Point out malaria parasites and leukocytes.
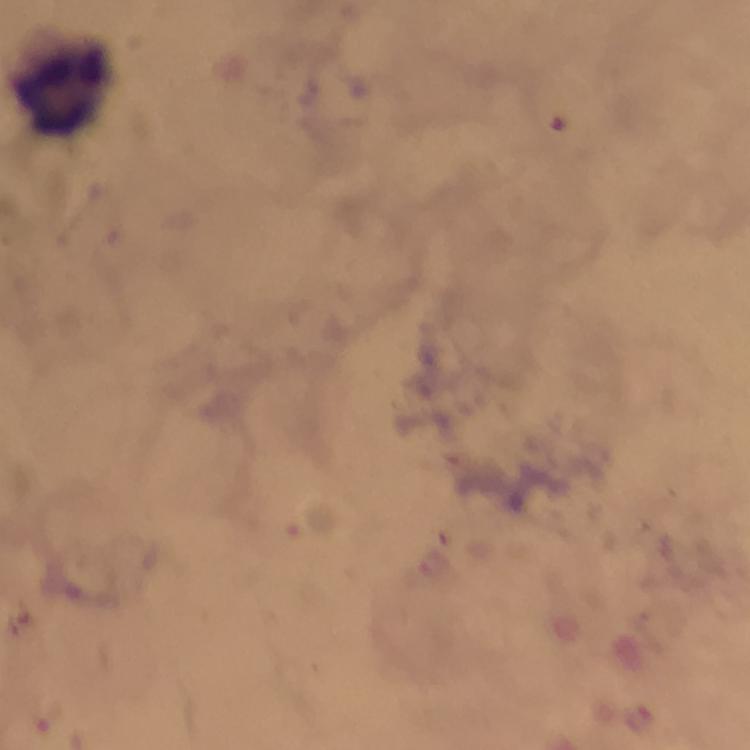
No malaria parasites seen.
Approximate centers as {x, y} in pixels.
Leukocytes: {64, 86}.

capture = smartphone camera through the microscope
cropped from = one field of view
preparation = thick smear
context = from a malaria diagnostic workup
immersion oil = applied
stain = Giemsa
magnification = 100x
image size = 750×750 pixels